State which cell type is depicted.
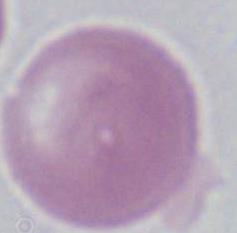

This is an erythrocyte.

Summary:
  - Magnification: 1000x
  - Modality: micrograph